Comment on the morphology of the erythrocytes.
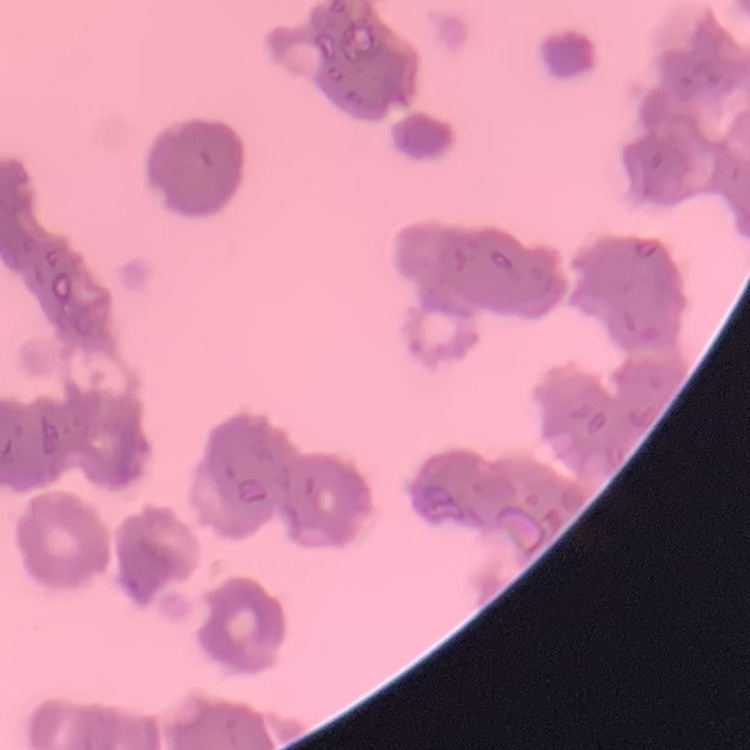
They show rouleaux formation.

{
  "stain": "Field's or Giemsa",
  "preparation": "thin blood smear",
  "image_type": "square crop of a larger photomicrograph"
}